Report the malaria status of this cell.
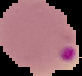

It is parasitized.

Summary:
  - Image type: segmented cell region with the area outside set to black
  - Image size: 82×76 pixels
  - Preparation: thin blood smear